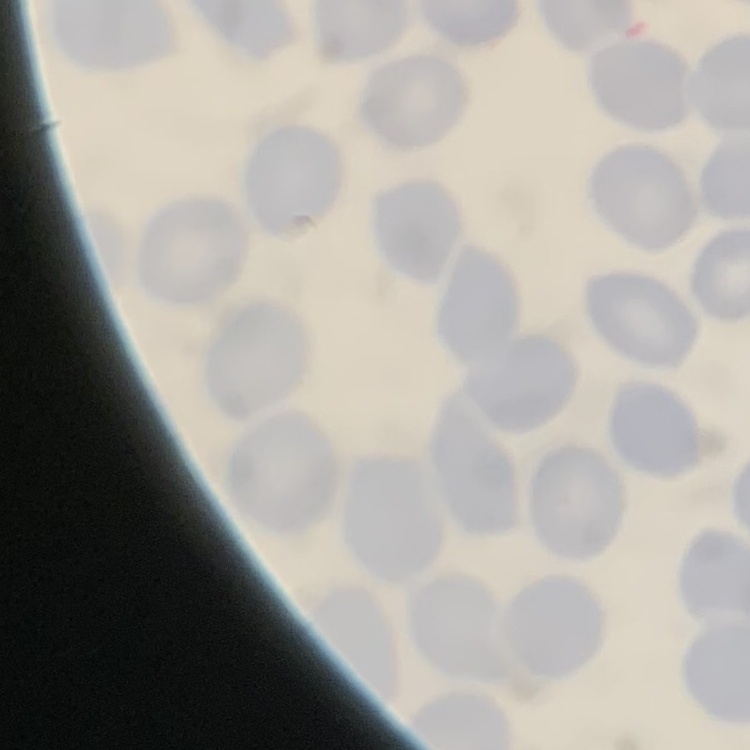 The erythrocytes exhibit no rouleaux formation. Thin blood film. Field's or Giemsa stain. Square crop of a larger photomicrograph.